Report the malaria status of this cell.
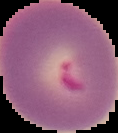

Parasitized.

preparation = thin blood smear
image type = segmented cell region with the area outside set to black
image size = 118×133 pixels